Locate every blood parasite and identify its species.
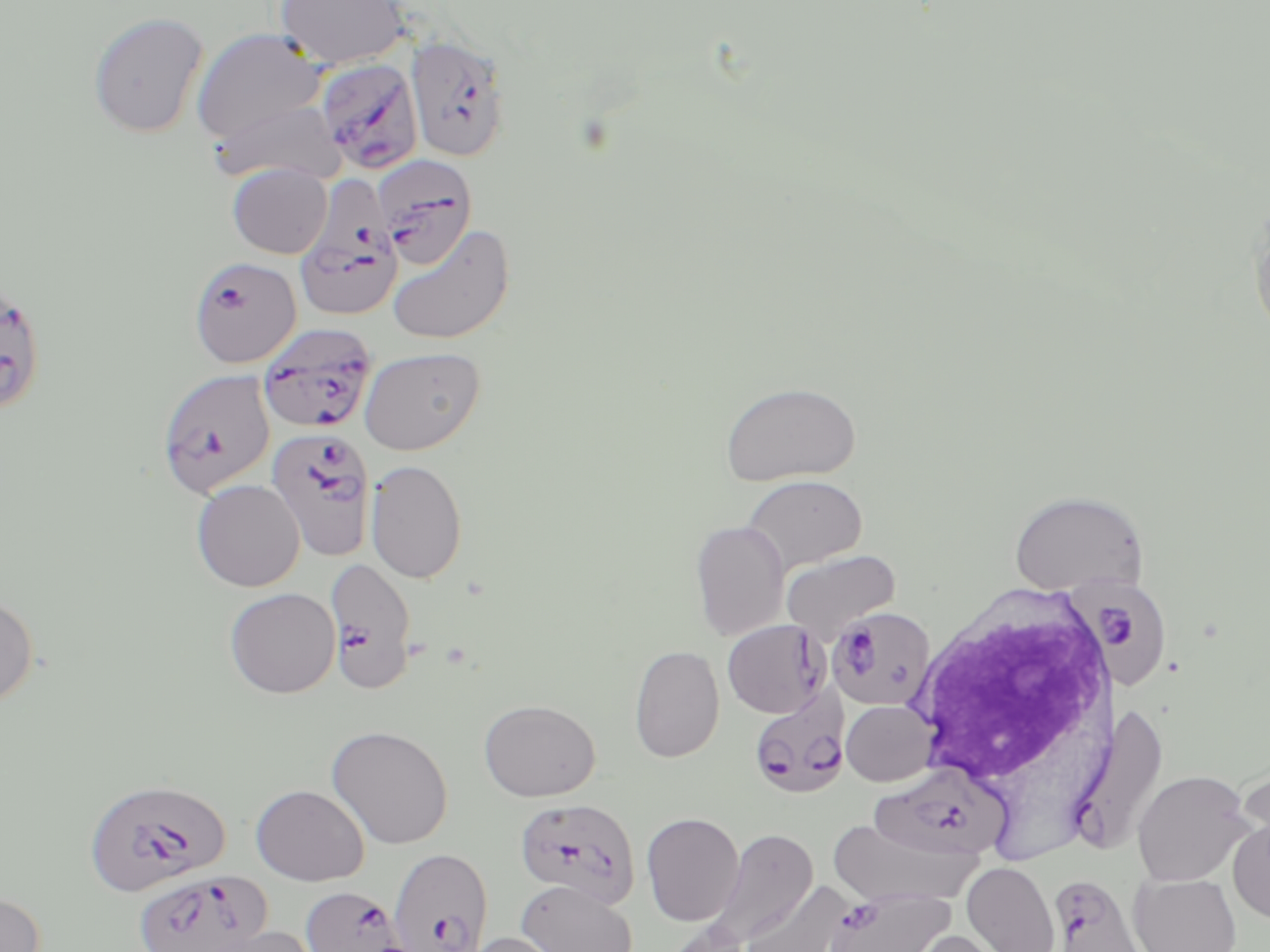
Approximate bounding boxes as (x1,y1)-(x2,y2) corner pairs in pixels.
Plasmodium falciparum-infected red blood cells: (406,35)-(510,162), (315,56)-(423,173), (371,153)-(478,269), (295,177)-(403,324), (188,256)-(301,369), (0,279)-(47,416), (257,322)-(376,433), (156,368)-(276,498), (266,427)-(376,562), (325,556)-(417,694), (1074,576)-(1176,689), (827,607)-(936,712), (722,619)-(829,718), (748,687)-(850,800), (1074,704)-(1170,854), (868,762)-(1012,863), (83,777)-(231,898), (514,797)-(641,909), (388,847)-(494,951), (131,871)-(272,952), (1051,877)-(1143,951), (301,886)-(404,952), (826,887)-(954,952).
No Plasmodium ovale, Plasmodium malariae, Plasmodium vivax, Babesia divergens, or Trypanosoma brucei observed.

Uninfected red blood cell locations: (274,0)-(410,69), (89,12)-(209,137), (192,28)-(330,148), (211,99)-(345,185), (228,163)-(332,259), (1249,204)-(1270,343), (387,223)-(516,345), (359,346)-(485,455), (720,381)-(861,485), (365,459)-(468,583), (741,474)-(868,574), (191,479)-(305,592), (1008,489)-(1148,598), (690,520)-(790,641), (781,549)-(901,643), (224,587)-(341,698), (0,592)-(39,710), (629,645)-(725,763), (479,699)-(600,801), (841,700)-(937,786), (326,724)-(453,849), (1132,770)-(1254,887), (251,783)-(369,886), (641,812)-(744,926), (826,818)-(977,909), (1228,818)-(1270,924), (711,828)-(817,945), (961,861)-(1061,952), (1129,873)-(1241,952), (517,880)-(638,952), (739,880)-(856,952), (0,890)-(46,952), (657,919)-(752,952), (198,925)-(321,952), (906,930)-(1010,952), (460,931)-(569,952). White blood cell locations: (905,585)-(1118,795). Slide-level diagnosis: Plasmodium falciparum. Image is 1270×952 pixels. May-Grünwald-Giemsa stain. Light microscopy. Thin blood smear. One field of a larger specimen. Captured at 1000x magnification.